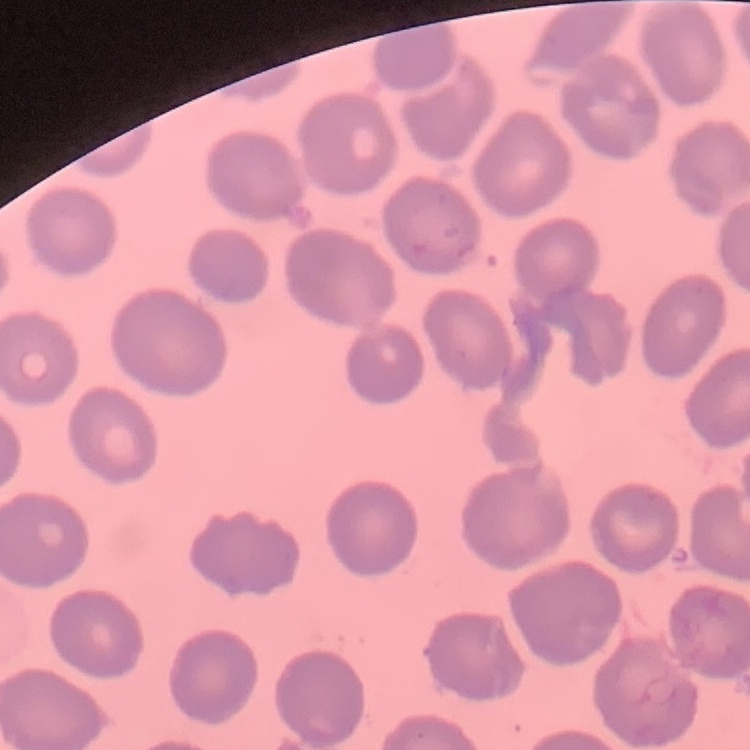
Summary:
  - Erythrocyte morphology: no rouleaux formation
  - Stain: Field's or Giemsa
  - Image type: one tile cut from a larger photomicrograph
  - Preparation: thin blood film